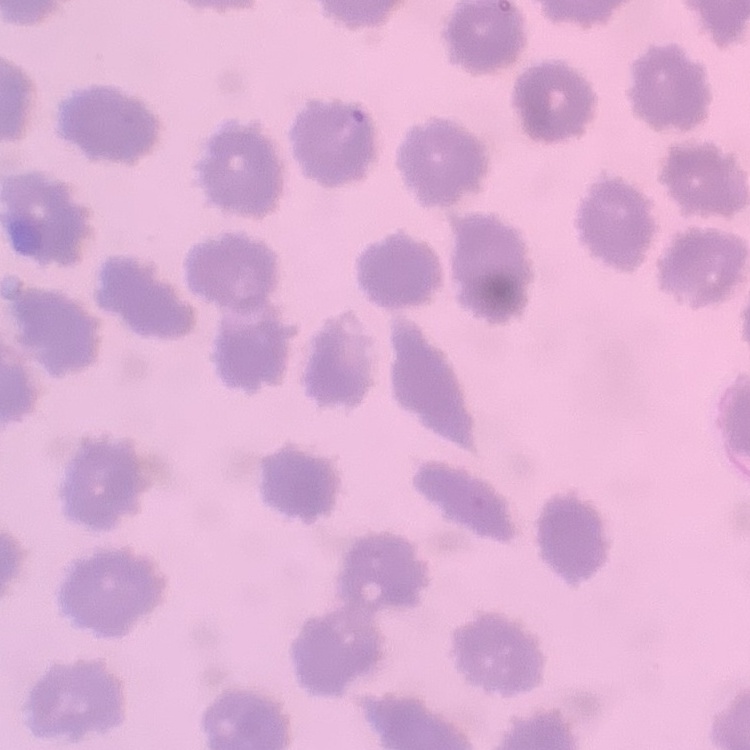
The erythrocytes exhibit no rouleaux formation. Thin peripheral smear. Stained with either Field's or Giemsa. Square crop of a larger photomicrograph.